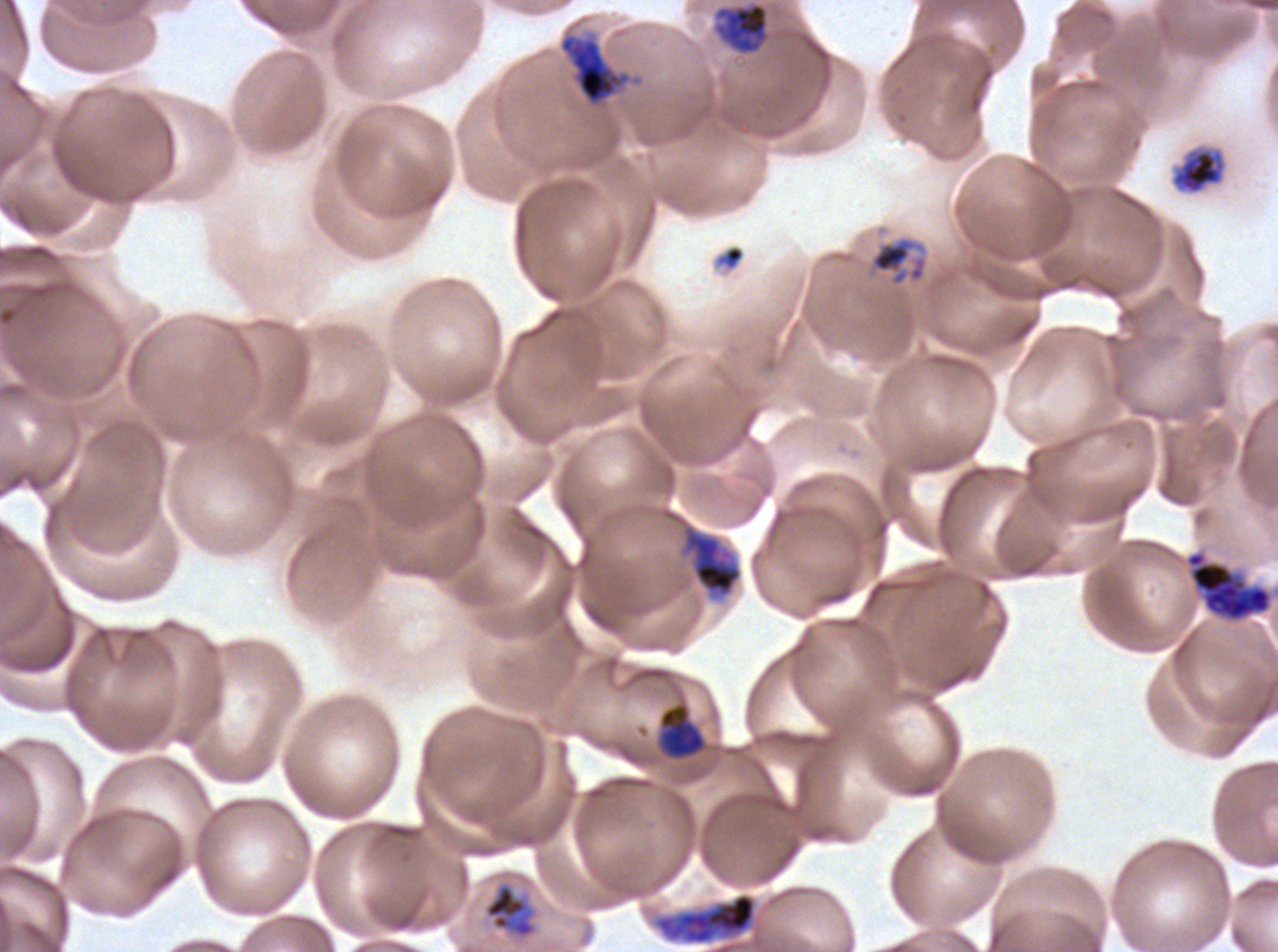
Approximate bounding rectangles given as corner coordinates in pixels from the top-left.
Summary:
  - Mid trophozoite locations: (x1=714, y1=1, x2=769, y2=55), (x1=1171, y1=147, x2=1227, y2=195), (x1=868, y1=236, x2=928, y2=287), (x1=659, y1=704, x2=706, y2=758), (x1=484, y1=883, x2=536, y2=938)
  - Late trophozoite locations: (x1=681, y1=522, x2=743, y2=600)
  - Debris locations: (x1=712, y1=243, x2=746, y2=275)
  - Early schizont locations: (x1=559, y1=35, x2=629, y2=104), (x1=1185, y1=549, x2=1273, y2=623), (x1=654, y1=892, x2=757, y2=946)
  - Life-cycle stages observed: mid trophozoite, late trophozoite, early schizont
  - Stain: Giemsa
  - Field of view: sub-image separated from a larger composite
  - Specimen: ex-vivo Plasmodium falciparum culture from a patient in The Gambia, grown for 24 to 48 hours
  - Image size: 1278×952 pixels
  - Preparation: thin blood film